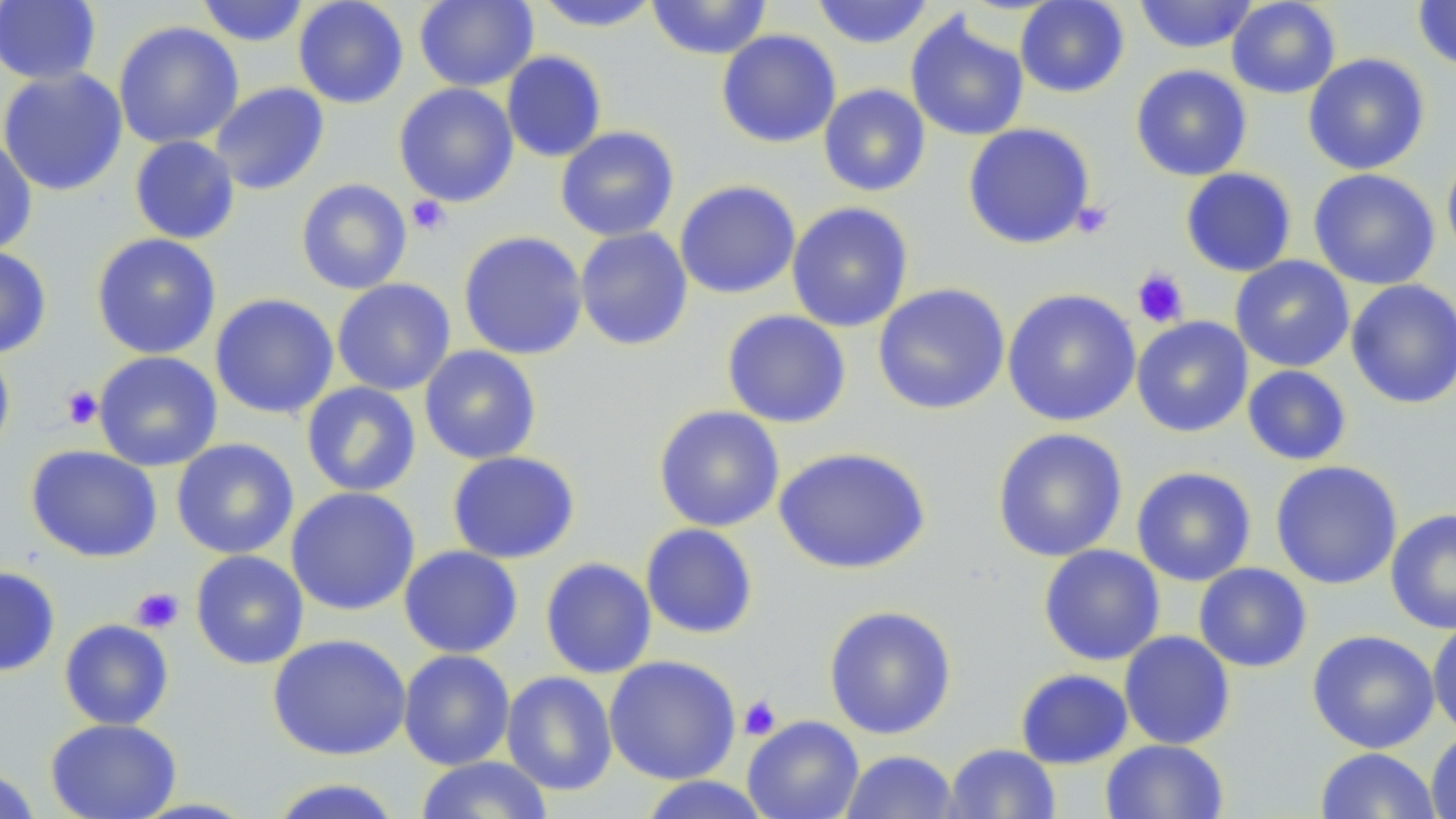
slide-level diagnosis = negative for blood parasites
magnification = 1000x
platelet locations = approximate bounding boxes as (x1,y1)-(x2,y2) corner pairs in pixels: (406,196)-(451,236), (1071,200)-(1115,239), (1132,268)-(1189,328), (61,385)-(103,430), (130,586)-(183,633), (738,695)-(781,741)
image size = 1456×819 pixels
modality = optical microscopy
uninfected red blood cell locations = approximate bounding boxes as (x1,y1)-(x2,y2) corner pairs in pixels: (0,0)-(101,86), (195,0)-(311,47), (293,0)-(409,109), (414,0)-(539,91), (646,0)-(772,59), (811,0)-(935,49), (1015,0)-(1129,98), (1133,0)-(1258,54), (1226,0)-(1341,99), (1412,0)-(1456,71), (532,1)-(662,32), (905,12)-(1029,142), (113,21)-(244,149), (716,29)-(841,149), (501,50)-(607,163), (1302,53)-(1430,176), (1130,64)-(1252,181), (0,68)-(128,196), (210,82)-(330,195), (393,83)-(519,207), (818,84)-(931,197), (962,123)-(1095,249), (555,125)-(680,242), (129,135)-(240,244), (0,137)-(37,256), (1441,146)-(1456,265), (1180,167)-(1297,277), (1308,168)-(1440,290), (296,178)-(412,295), (674,179)-(801,299), (786,202)-(914,332), (575,226)-(693,351), (459,231)-(588,360), (91,233)-(222,359), (0,246)-(52,358), (1230,255)-(1354,373), (332,278)-(456,396), (1346,279)-(1456,409), (872,283)-(1011,415), (1002,288)-(1142,427), (209,293)-(339,420), (722,309)-(852,429), (1131,316)-(1253,438), (0,343)-(15,461), (419,345)-(542,465), (93,351)-(223,471), (1241,364)-(1353,466), (301,381)-(421,497), (653,405)-(785,532), (991,427)-(1128,563), (170,438)-(299,560), (25,445)-(163,563), (773,446)-(931,575), (447,450)-(581,564), (1270,460)-(1403,590), (1131,467)-(1257,587), (286,486)-(420,616), (1386,508)-(1456,635), (640,523)-(759,640), (398,544)-(524,659), (1038,544)-(1165,666), (190,550)-(309,670), (540,557)-(657,679), (1193,563)-(1312,673), (0,565)-(60,677), (823,604)-(958,740), (1427,618)-(1456,738), (59,619)-(174,730), (1306,629)-(1440,753), (1119,631)-(1236,750), (267,633)-(412,761), (398,649)-(516,770), (604,655)-(741,784), (1015,668)-(1133,769), (501,670)-(618,796), (742,715)-(864,819), (45,717)-(181,819), (1426,729)-(1456,819), (1101,739)-(1229,818), (944,743)-(1061,818), (1315,747)-(1440,819), (839,750)-(960,818), (415,756)-(556,819), (0,766)-(41,819), (637,776)-(775,818), (265,777)-(404,819)
stain = May-Grünwald-Giemsa
preparation = thin blood smear
field of view = single